Describe the morphology of the red blood cells.
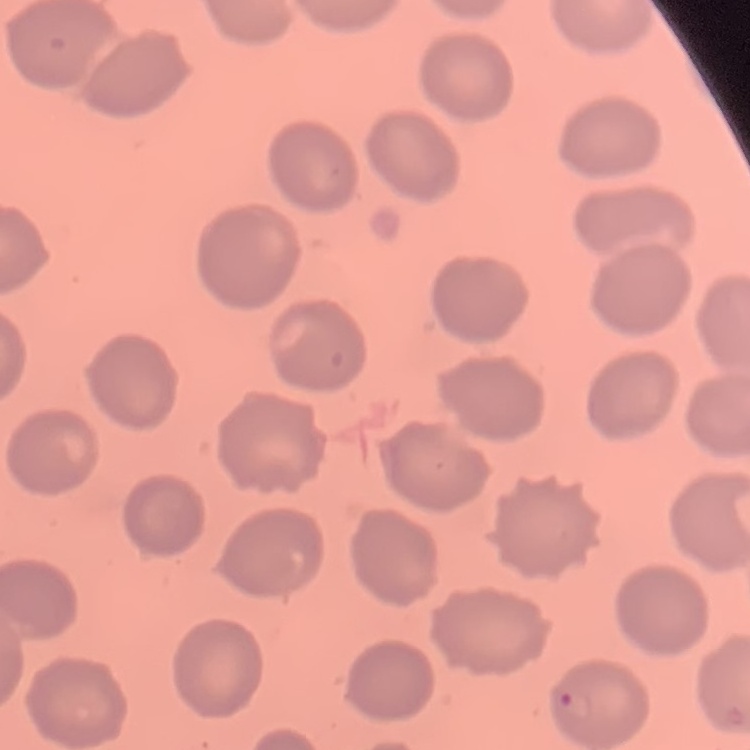

No rouleaux formation.

image type = square crop of a larger photomicrograph
preparation = thin blood smear
stain = Field's or Giemsa